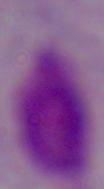
Micrograph. A trichomonad is seen. Captured at 1000x magnification.